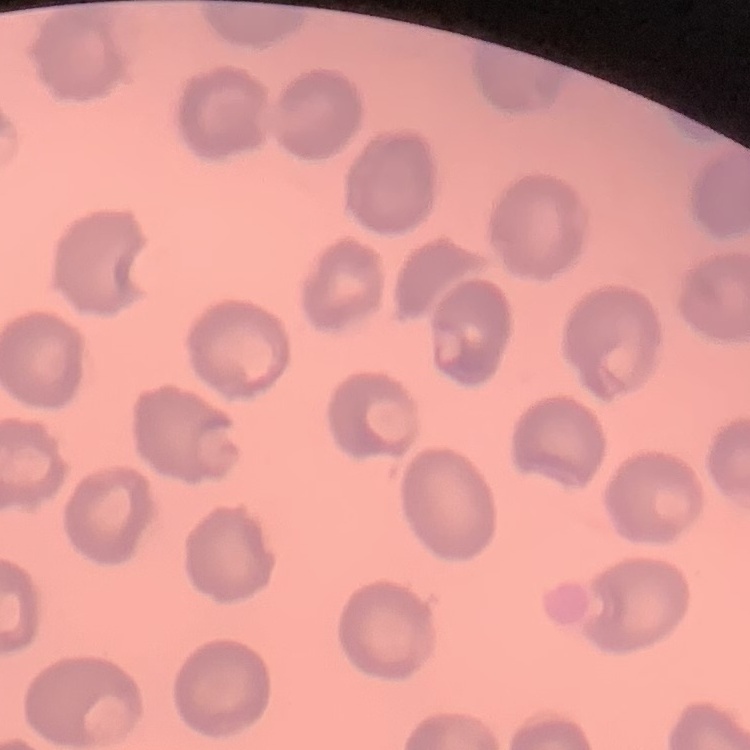 The erythrocytes show no rouleaux formation. Field's or Giemsa stain. Thin peripheral smear. Square crop of a larger photomicrograph.